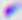

magnification = 400x
modality = micrograph
identification = Toxoplasma gondii